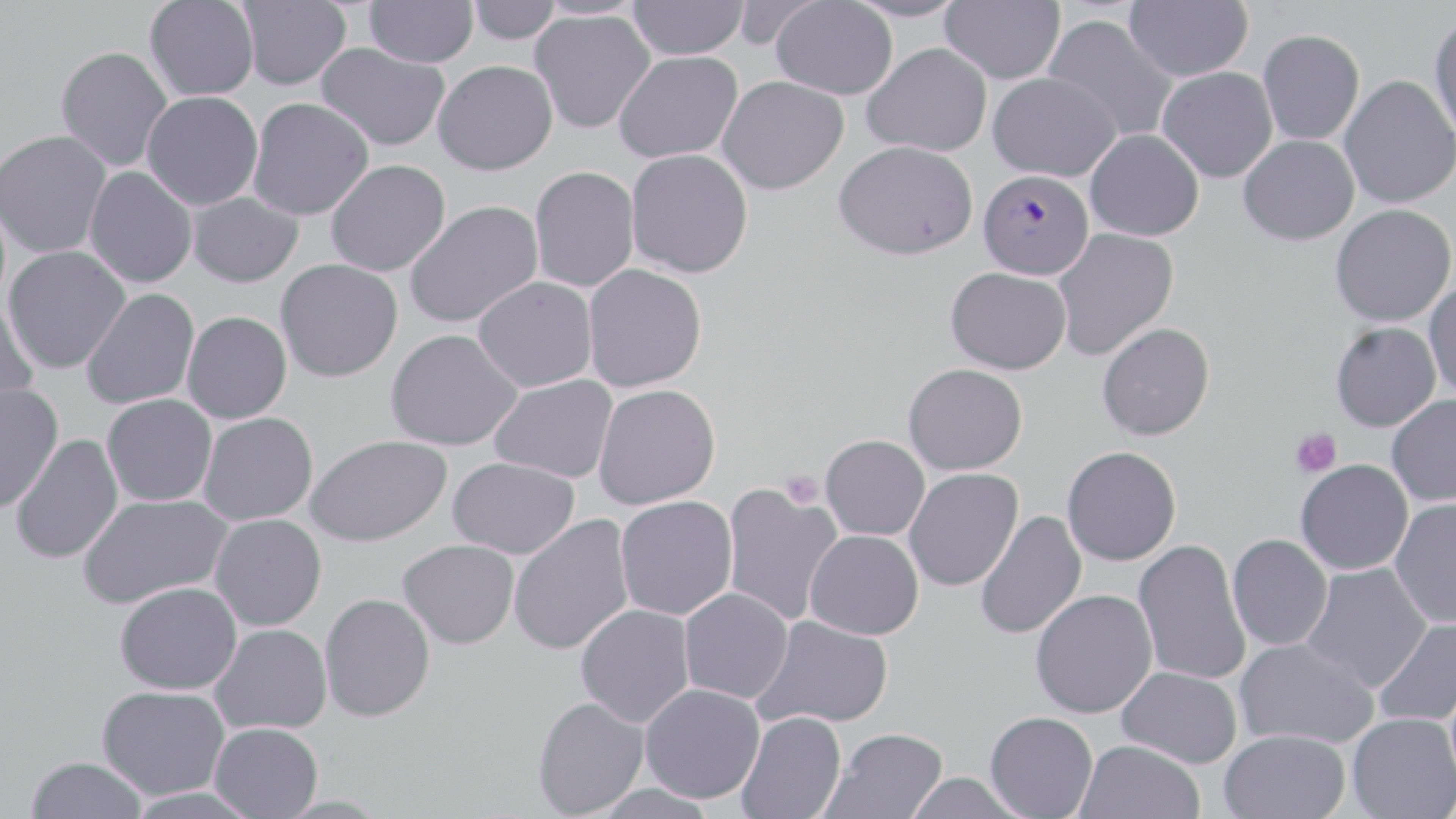
Approximate bounding boxes as named x1/y1/x2/y2 corners in pixels. Uninfected red blood cell locations: (x1=144, y1=0, x2=259, y2=101), (x1=236, y1=0, x2=352, y2=91), (x1=364, y1=0, x2=478, y2=69), (x1=466, y1=0, x2=561, y2=44), (x1=844, y1=0, x2=967, y2=23), (x1=939, y1=0, x2=1065, y2=84), (x1=628, y1=1, x2=749, y2=60), (x1=770, y1=1, x2=898, y2=100), (x1=1123, y1=1, x2=1253, y2=81), (x1=530, y1=9, x2=655, y2=134), (x1=1042, y1=14, x2=1179, y2=143), (x1=1428, y1=15, x2=1456, y2=143), (x1=1257, y1=29, x2=1365, y2=145), (x1=316, y1=42, x2=450, y2=152), (x1=862, y1=42, x2=992, y2=157), (x1=56, y1=46, x2=173, y2=172), (x1=614, y1=51, x2=743, y2=163), (x1=432, y1=60, x2=558, y2=176), (x1=1157, y1=66, x2=1277, y2=183), (x1=987, y1=72, x2=1121, y2=182), (x1=1339, y1=75, x2=1455, y2=209), (x1=717, y1=76, x2=849, y2=195), (x1=141, y1=91, x2=263, y2=210), (x1=248, y1=97, x2=374, y2=221), (x1=1085, y1=129, x2=1204, y2=241), (x1=0, y1=130, x2=112, y2=258), (x1=1238, y1=135, x2=1360, y2=245), (x1=834, y1=140, x2=978, y2=260), (x1=626, y1=149, x2=754, y2=278), (x1=325, y1=159, x2=450, y2=277), (x1=529, y1=166, x2=640, y2=292), (x1=83, y1=167, x2=197, y2=289), (x1=188, y1=192, x2=303, y2=288), (x1=404, y1=200, x2=543, y2=328), (x1=1330, y1=204, x2=1455, y2=326), (x1=1051, y1=227, x2=1178, y2=361), (x1=2, y1=245, x2=130, y2=374), (x1=275, y1=259, x2=403, y2=382), (x1=582, y1=264, x2=707, y2=392), (x1=946, y1=267, x2=1072, y2=374), (x1=473, y1=277, x2=597, y2=392), (x1=1424, y1=279, x2=1456, y2=399), (x1=81, y1=288, x2=199, y2=410), (x1=0, y1=302, x2=40, y2=418), (x1=182, y1=311, x2=292, y2=424), (x1=1096, y1=321, x2=1215, y2=440), (x1=1330, y1=322, x2=1441, y2=432), (x1=385, y1=329, x2=523, y2=451), (x1=903, y1=363, x2=1028, y2=475), (x1=489, y1=375, x2=618, y2=484), (x1=0, y1=383, x2=64, y2=512), (x1=593, y1=384, x2=720, y2=510), (x1=101, y1=394, x2=217, y2=506), (x1=1386, y1=395, x2=1456, y2=507), (x1=198, y1=412, x2=318, y2=526), (x1=10, y1=434, x2=124, y2=564), (x1=305, y1=434, x2=452, y2=547), (x1=820, y1=435, x2=930, y2=540), (x1=1062, y1=446, x2=1181, y2=566), (x1=447, y1=457, x2=580, y2=559), (x1=1295, y1=460, x2=1413, y2=575), (x1=903, y1=468, x2=1023, y2=591), (x1=720, y1=484, x2=843, y2=626), (x1=77, y1=493, x2=232, y2=609), (x1=615, y1=496, x2=738, y2=621), (x1=1389, y1=497, x2=1456, y2=629), (x1=974, y1=510, x2=1087, y2=640), (x1=209, y1=513, x2=327, y2=631), (x1=508, y1=517, x2=634, y2=655), (x1=805, y1=530, x2=924, y2=640), (x1=1227, y1=534, x2=1333, y2=652), (x1=398, y1=540, x2=519, y2=649), (x1=1132, y1=540, x2=1252, y2=686), (x1=1300, y1=563, x2=1432, y2=694), (x1=114, y1=581, x2=242, y2=695), (x1=678, y1=588, x2=793, y2=704), (x1=1030, y1=589, x2=1157, y2=718), (x1=319, y1=593, x2=436, y2=722), (x1=575, y1=604, x2=695, y2=728), (x1=752, y1=615, x2=893, y2=730), (x1=1373, y1=616, x2=1456, y2=727), (x1=209, y1=623, x2=332, y2=735), (x1=1234, y1=637, x2=1379, y2=749), (x1=1116, y1=666, x2=1242, y2=768), (x1=640, y1=684, x2=765, y2=804), (x1=96, y1=686, x2=230, y2=800), (x1=532, y1=697, x2=649, y2=818), (x1=736, y1=711, x2=846, y2=819), (x1=985, y1=711, x2=1098, y2=819), (x1=1347, y1=712, x2=1455, y2=819), (x1=209, y1=722, x2=323, y2=819), (x1=821, y1=728, x2=948, y2=819), (x1=1219, y1=729, x2=1350, y2=818), (x1=1073, y1=739, x2=1205, y2=819), (x1=27, y1=756, x2=147, y2=818), (x1=901, y1=772, x2=1030, y2=819), (x1=590, y1=783, x2=719, y2=819). Plasmodium falciparum-infected red blood cell locations: (x1=978, y1=169, x2=1093, y2=280). Platelet locations: (x1=1291, y1=428, x2=1342, y2=478), (x1=781, y1=470, x2=825, y2=509). Slide-level diagnosis: Plasmodium falciparum. Image is 1456×819 pixels. Thin blood film. Captured at 1000x magnification. May-Grünwald-Giemsa-stained preparation. One field of a larger specimen. Optical microscopy.